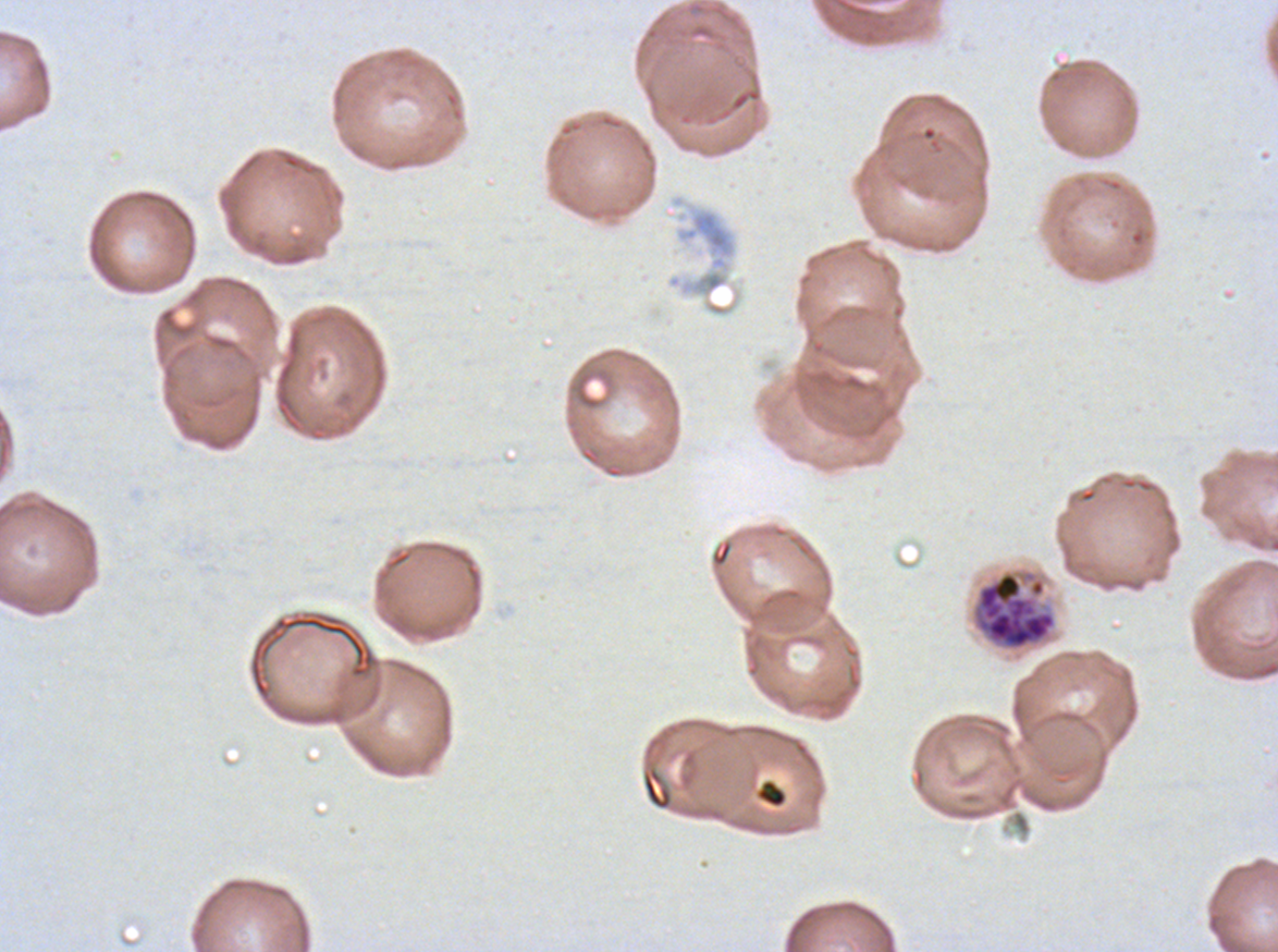
Approximate bounding boxes as (x1, y1, x2, y2) in pixels. Late schizont locations: (970, 568, 1058, 652). Debris locations: (641, 767, 673, 811), (756, 778, 788, 809). Image is 1278×952 pixels. Giemsa-stained preparation. One sub-image of a larger composite. Ex-vivo Plasmodium falciparum culture from a patient in The Gambia, grown for 24 to 48 hours. Thin blood smear.